Point out each malaria parasite.
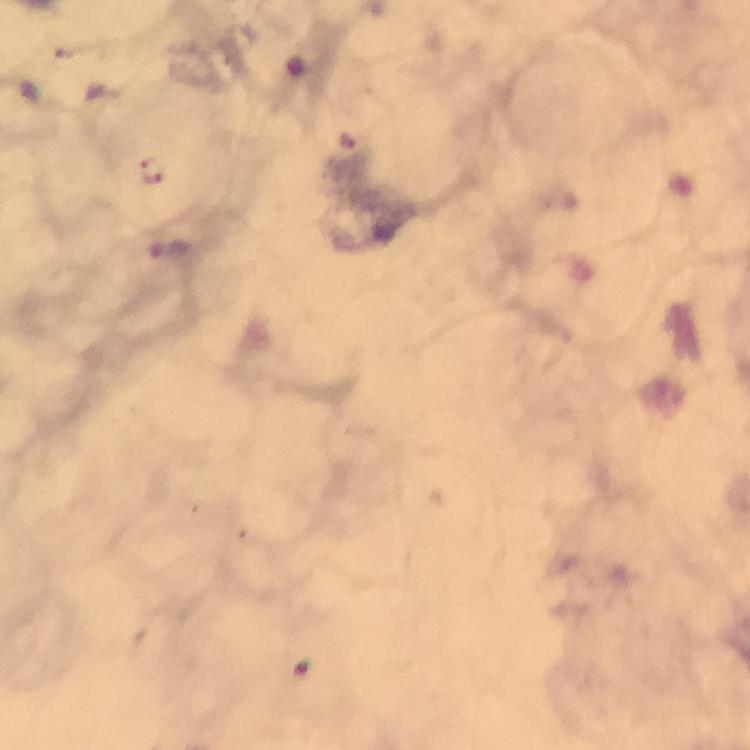

Approximate object centers, in pixels from the top-left corner.
Malaria parasites: (x=346, y=139), (x=156, y=172).

From a diagnostic examination for malaria. Photographed through the microscope with a smartphone camera. Thick smear. At 100x magnification. Giemsa-stained preparation. Immersion oil applied. Image is 750×750 pixels. A crop from one field of view.